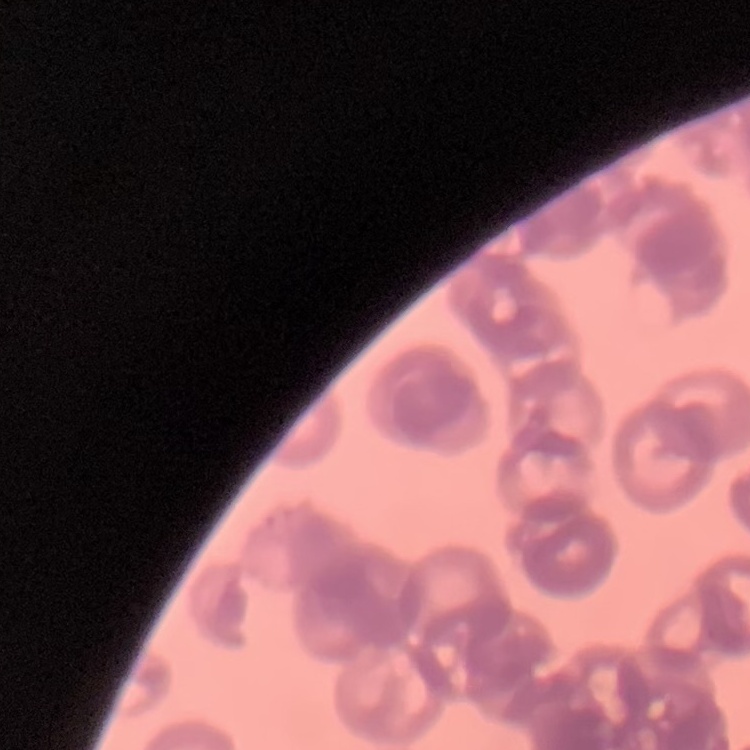

Summary:
  - Erythrocyte morphology: rouleaux formation
  - Stain: Field's or Giemsa
  - Image type: square crop of a larger photomicrograph
  - Preparation: thin blood film